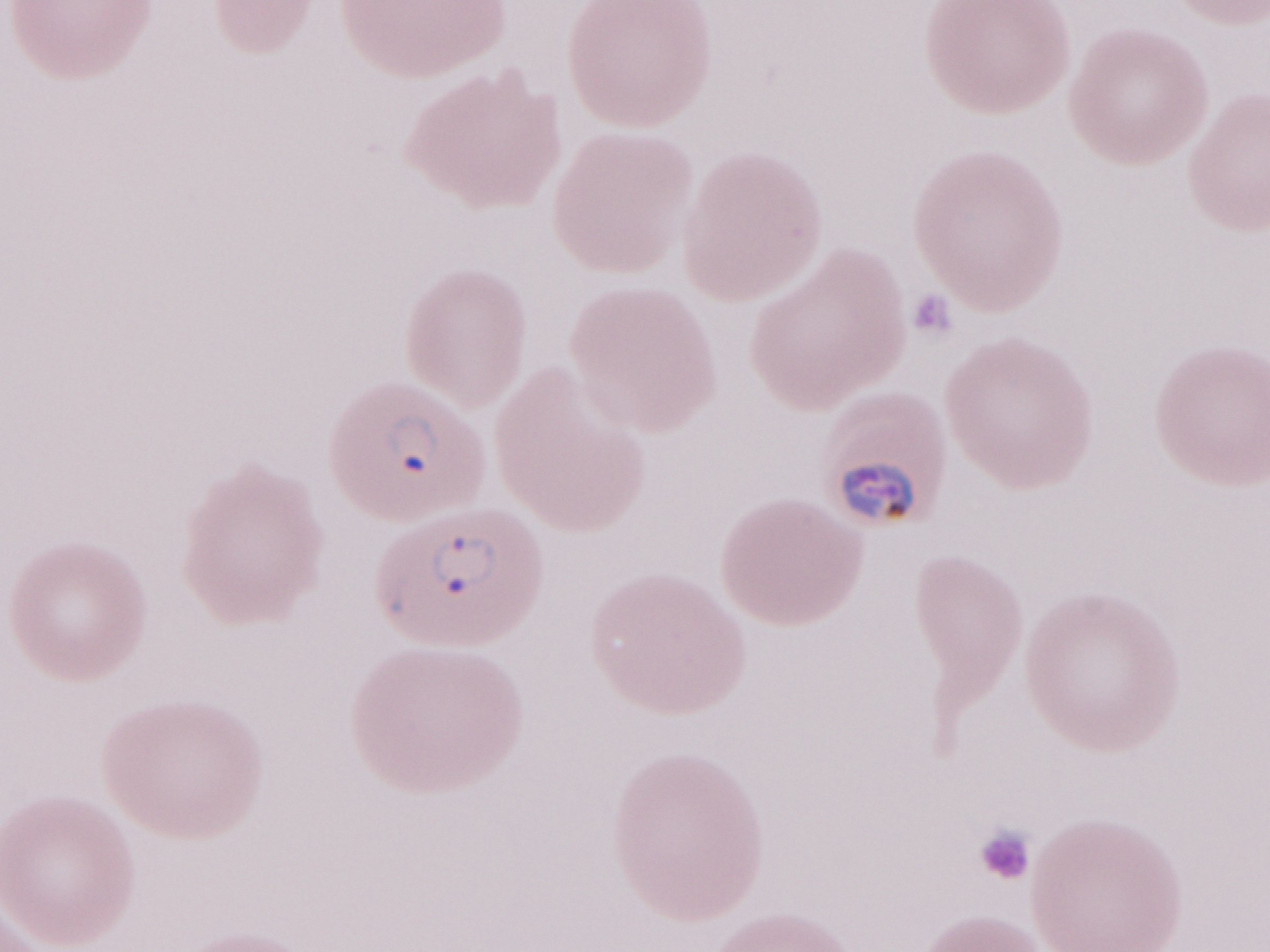
Image is 1270×952 pixels. Olympus BX43 microscope, Olympus DP73 camera. Malaria diagnosis (patient-level): positive. May-Grünwald-Giemsa (MGG) stain. One field of this slide. Thin blood film. Magnification: 1,000x.